Report the malaria status of this cell.
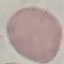
It is uninfected.

Giemsa-stained preparation. Acquired by smartphone through the microscope eyepiece. Thin smear of blood. Cell patch, automatically extracted from a larger field of view and resized to 64 × 64 pixels.